Locate every uninfected red blood cell.
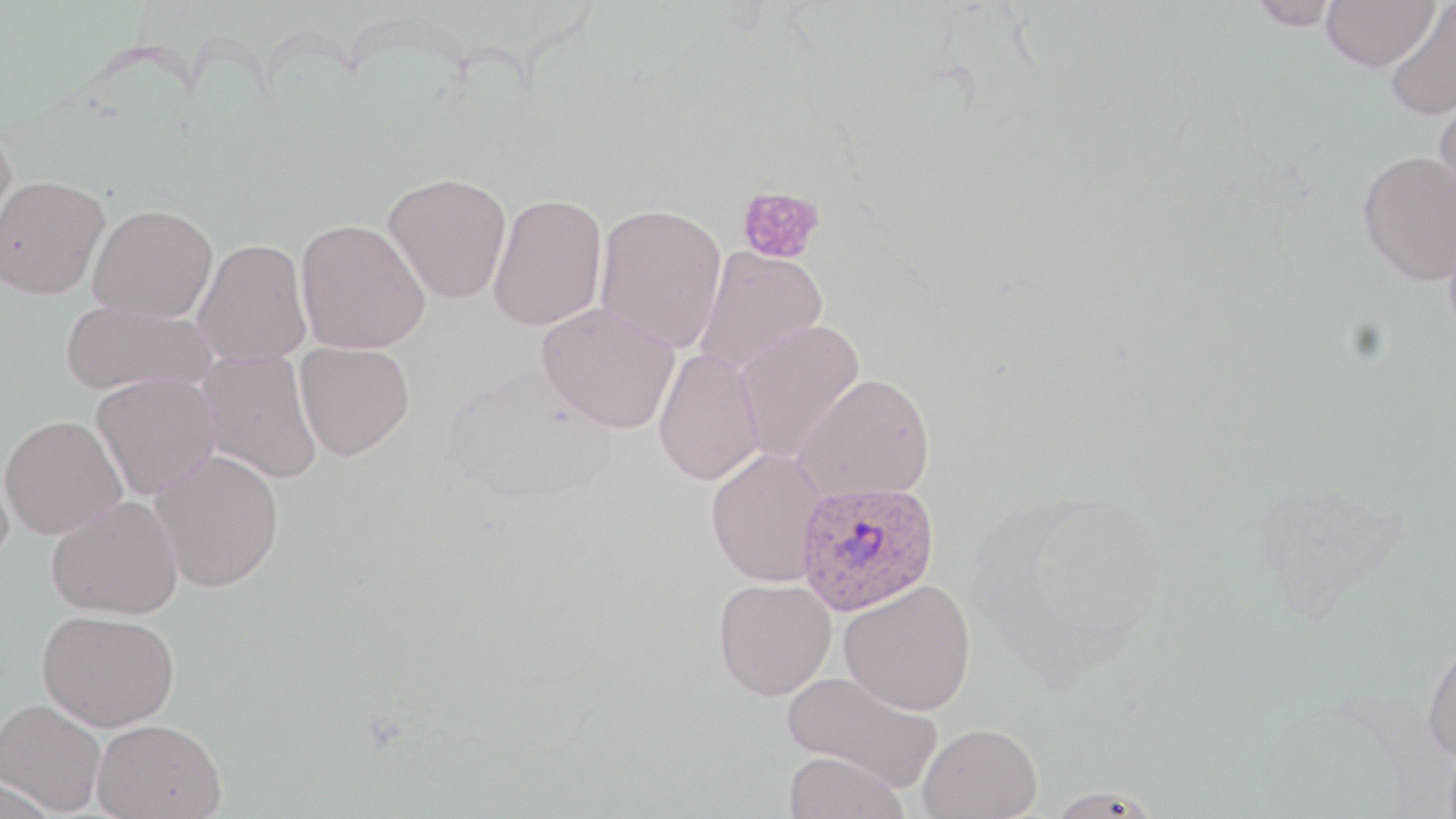

Approximate bounding boxes as named x1/y1/x2/y2 corners in pixels.
Uninfected red blood cells: (x1=1248, y1=0, x2=1342, y2=30), (x1=1321, y1=0, x2=1438, y2=72), (x1=1385, y1=1, x2=1456, y2=121), (x1=1433, y1=90, x2=1456, y2=212), (x1=0, y1=127, x2=17, y2=257), (x1=1357, y1=151, x2=1456, y2=285), (x1=383, y1=172, x2=512, y2=304), (x1=0, y1=174, x2=110, y2=300), (x1=488, y1=192, x2=608, y2=331), (x1=594, y1=202, x2=728, y2=353), (x1=87, y1=204, x2=218, y2=322), (x1=295, y1=218, x2=431, y2=354), (x1=192, y1=238, x2=312, y2=367), (x1=694, y1=246, x2=829, y2=376), (x1=60, y1=300, x2=216, y2=398), (x1=537, y1=302, x2=680, y2=433), (x1=733, y1=319, x2=866, y2=463), (x1=294, y1=342, x2=415, y2=461), (x1=654, y1=347, x2=765, y2=486), (x1=196, y1=349, x2=323, y2=484), (x1=91, y1=373, x2=221, y2=500), (x1=794, y1=373, x2=936, y2=502), (x1=0, y1=415, x2=127, y2=540), (x1=0, y1=445, x2=16, y2=573), (x1=704, y1=448, x2=830, y2=586), (x1=150, y1=449, x2=285, y2=592), (x1=46, y1=495, x2=184, y2=620), (x1=713, y1=578, x2=836, y2=700), (x1=839, y1=579, x2=976, y2=716), (x1=36, y1=609, x2=180, y2=731), (x1=1421, y1=636, x2=1456, y2=762), (x1=782, y1=668, x2=944, y2=792), (x1=0, y1=699, x2=107, y2=815), (x1=91, y1=718, x2=228, y2=818), (x1=918, y1=722, x2=1041, y2=819), (x1=784, y1=751, x2=908, y2=819), (x1=1045, y1=785, x2=1163, y2=818).

Plasmodium ovale-infected red blood cell locations: (x1=796, y1=478, x2=941, y2=615). Platelet locations: (x1=737, y1=186, x2=826, y2=265). Slide-level diagnosis: Plasmodium ovale. Optical microscopy. 1000x magnification. Image is 1456×819 pixels. Single field of view. Thin blood film. May-Grünwald-Giemsa-stained preparation.